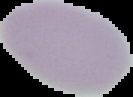

image size = 133×97 pixels
image type = segmented cell region with the area outside set to black
malaria status = uninfected
preparation = thin blood smear